Assess the morphology of the erythrocytes.
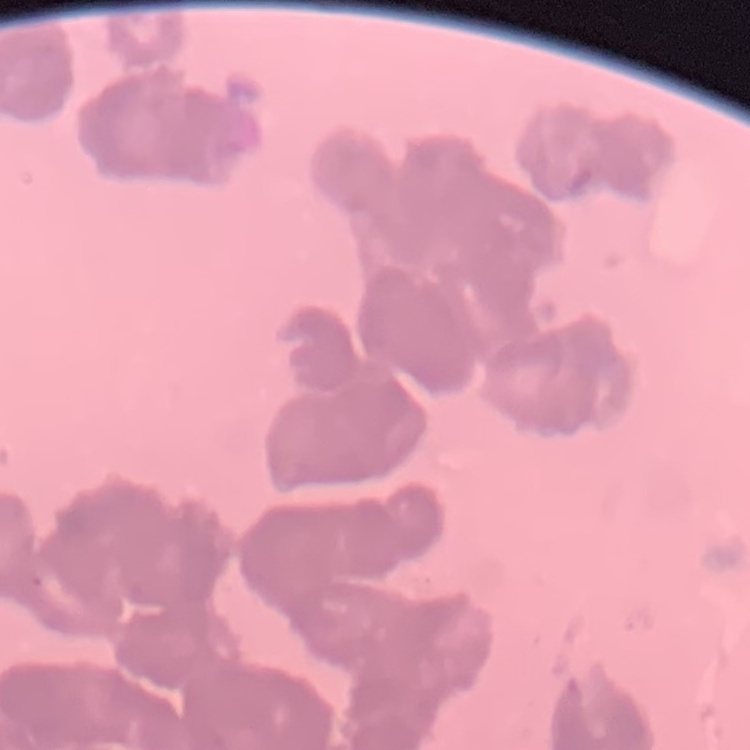

Rouleaux formation.

One tile cut from a larger photomicrograph. Thin blood film. Stained with either Field's or Giemsa.